Name the blood parasite species.
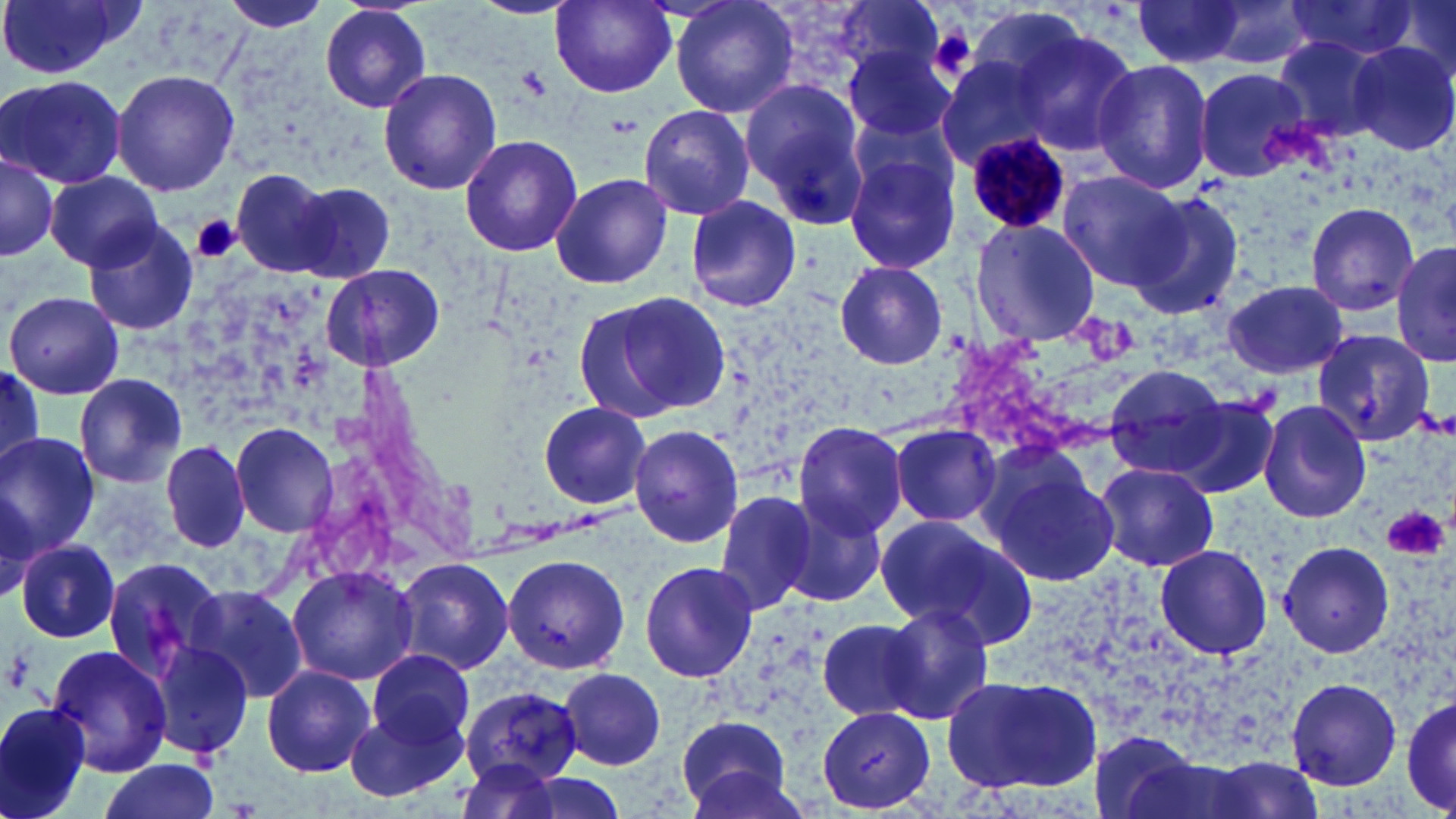

Plasmodium malariae.

Summary:
  - Coordinate format: approximate bounding boxes as [x1, y1, x2, y2] in pixels
  - Plasmodium malariae-infected red blood cell locations: [965, 131, 1070, 236]
  - Uninfected red blood cell locations: [0, 0, 141, 80], [218, 0, 334, 37], [548, 0, 679, 98], [669, 0, 801, 120], [1127, 0, 1248, 65], [1192, 0, 1319, 71], [1377, 0, 1456, 84], [1278, 2, 1421, 60], [318, 4, 433, 113], [1012, 29, 1138, 155], [1270, 35, 1390, 144], [1344, 40, 1456, 157], [845, 44, 958, 143], [934, 52, 1060, 166], [1090, 57, 1215, 195], [111, 67, 240, 197], [378, 67, 502, 195], [1195, 67, 1316, 182], [0, 72, 130, 188], [741, 77, 871, 220], [637, 105, 756, 219], [458, 132, 584, 259], [1, 146, 61, 263], [843, 149, 960, 275], [230, 169, 335, 277], [550, 170, 675, 290], [1057, 170, 1188, 291], [46, 172, 162, 270], [292, 184, 397, 282], [1124, 190, 1247, 321], [684, 194, 803, 313], [1304, 203, 1421, 316], [968, 217, 1100, 347], [81, 218, 201, 336], [1391, 240, 1455, 367], [833, 261, 949, 370], [321, 263, 445, 372], [1220, 279, 1350, 379], [6, 291, 124, 399], [580, 291, 732, 419], [1309, 326, 1436, 446], [1103, 363, 1233, 479], [0, 369, 45, 471], [73, 374, 186, 487], [1167, 396, 1280, 500], [1257, 398, 1374, 525], [536, 401, 654, 510], [229, 421, 337, 537], [792, 422, 908, 538], [889, 422, 1001, 527], [627, 426, 745, 546], [0, 432, 100, 557], [159, 439, 251, 554], [975, 447, 1121, 588], [1093, 462, 1219, 572], [713, 487, 822, 613], [777, 497, 889, 608], [878, 514, 1036, 647], [1280, 538, 1393, 659], [16, 540, 119, 642], [1152, 543, 1274, 661], [502, 552, 629, 675], [101, 553, 229, 682], [395, 557, 514, 676], [639, 558, 759, 683], [285, 562, 417, 685], [187, 583, 309, 704], [880, 601, 993, 723], [813, 619, 925, 721], [148, 640, 255, 760], [45, 643, 173, 776], [367, 648, 475, 749], [261, 665, 374, 776], [559, 669, 666, 770], [942, 672, 1101, 793], [1285, 677, 1402, 789], [458, 685, 584, 788], [1400, 689, 1456, 817], [344, 695, 469, 807], [0, 699, 94, 819], [816, 706, 936, 814], [674, 713, 796, 816], [96, 758, 221, 819], [482, 769, 636, 819]
  - Platelet locations: [930, 22, 974, 77], [517, 65, 550, 98], [602, 112, 642, 138], [191, 214, 241, 264], [1382, 506, 1448, 561], [2, 639, 36, 693]
  - Magnification: 1000x
  - Modality: optical microscopy
  - Stain: May-Grünwald-Giemsa
  - Image size: 1456×819 pixels
  - Preparation: thin blood film
  - Field of view: one of a larger specimen